Give the position of every leukocyte visible.
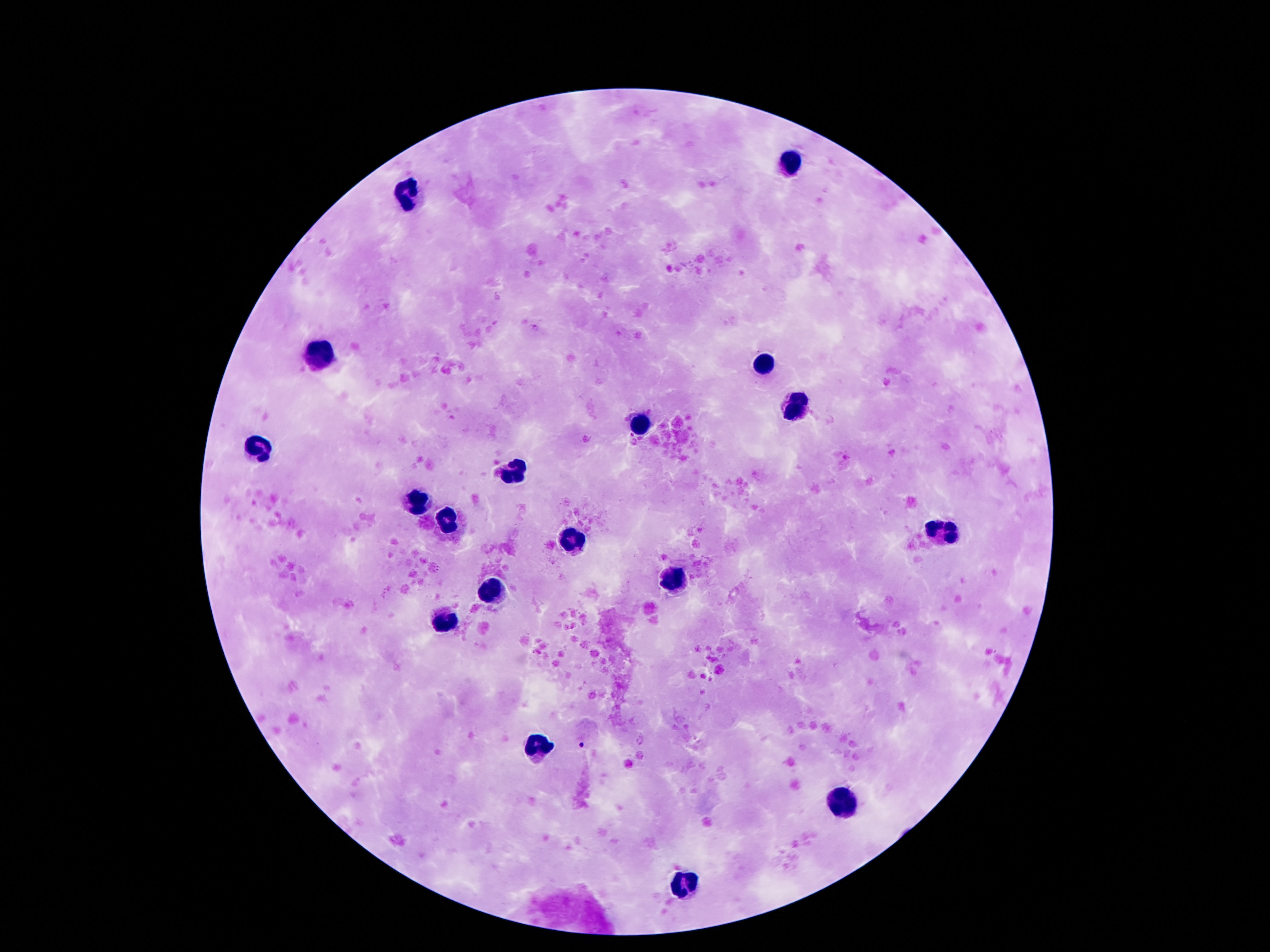
Approximate centers as [x, y] in pixels.
Leukocytes: [790, 162], [406, 196], [322, 353], [763, 366], [790, 405], [639, 425], [259, 450], [511, 473], [417, 500], [446, 523], [942, 533], [570, 540], [673, 578], [492, 591], [446, 626], [538, 745], [845, 803], [685, 886].

Summary:
  - Image size: 1270×952 pixels
  - Field of view: single
  - Patient malaria status: not infected
  - Preparation: thick blood film
  - Capture: smartphone camera through the microscope eyepiece
  - Magnification: 100x
  - Stain: Giemsa